Report the malaria status of this cell.
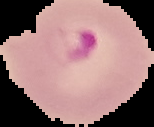
Parasitized.

image type = cell region segmented out of the field of view; surrounding area masked to black
image size = 154×127 pixels
preparation = thin blood film